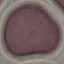 Malaria status: uninfected. Photographed with a smartphone camera at the microscope eyepiece. Thin blood film. Automatically extracted cell patch, resized to 64 × 64 pixels. Giemsa-stained preparation.